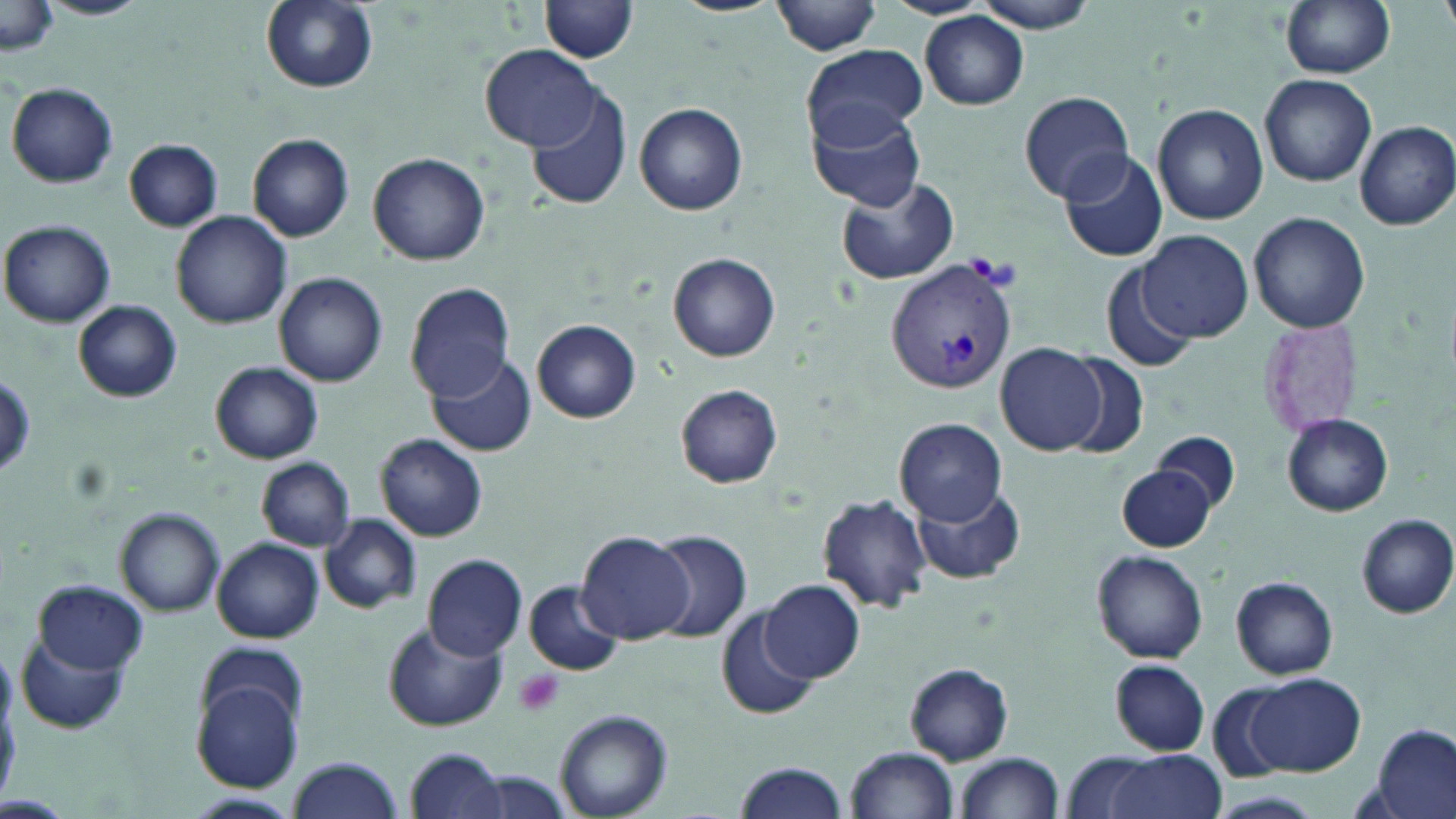

slide-level diagnosis = Plasmodium vivax
image size = 1456×819 pixels
field of view = one of a larger specimen
platelet locations = approximate bounding boxes as [x1, y1, x2, y2] in pixels: [512, 667, 565, 719]
uninfected red blood cell locations = approximate bounding boxes as [x1, y1, x2, y2] in pixels: [41, 0, 148, 20], [259, 0, 378, 92], [1279, 0, 1393, 79], [540, 1, 639, 63], [771, 1, 883, 55], [971, 1, 1102, 33], [1, 2, 61, 60], [920, 13, 1030, 109], [481, 43, 599, 149], [802, 43, 927, 150], [1259, 72, 1377, 186], [6, 80, 117, 188], [525, 85, 635, 212], [1020, 90, 1135, 203], [635, 102, 749, 214], [1153, 103, 1269, 223], [809, 106, 928, 210], [1354, 121, 1456, 231], [247, 133, 354, 241], [125, 141, 223, 230], [1058, 147, 1167, 263], [368, 151, 491, 265], [836, 175, 959, 286], [1247, 211, 1370, 334], [171, 212, 293, 328], [1, 219, 118, 327], [1139, 230, 1252, 342], [668, 252, 781, 361], [1099, 259, 1201, 374], [275, 273, 388, 387], [406, 283, 514, 401], [74, 300, 181, 402], [533, 318, 642, 422], [995, 343, 1104, 455], [428, 351, 536, 457], [1057, 353, 1152, 461], [209, 361, 323, 465], [0, 368, 34, 481], [676, 384, 782, 488], [1282, 415, 1393, 516], [895, 416, 1007, 525], [1153, 431, 1241, 515], [376, 434, 487, 542], [257, 457, 354, 551], [1116, 465, 1217, 551], [912, 481, 1024, 585], [816, 495, 933, 613], [114, 506, 226, 617], [1356, 513, 1456, 619], [319, 514, 422, 614], [648, 530, 752, 644], [577, 531, 694, 644], [213, 537, 324, 643], [1093, 549, 1209, 663], [424, 553, 528, 661], [1229, 576, 1339, 680], [760, 578, 865, 684], [35, 581, 147, 675], [525, 583, 622, 676], [717, 607, 821, 723], [383, 618, 506, 730], [15, 627, 132, 736], [1109, 661, 1209, 755], [904, 662, 1014, 763], [193, 672, 304, 794], [1244, 673, 1364, 774], [555, 710, 671, 819], [1370, 724, 1455, 819], [847, 746, 960, 818], [406, 748, 508, 819], [953, 752, 1065, 819], [1096, 752, 1223, 819], [288, 757, 404, 819], [731, 762, 843, 819], [475, 771, 571, 818], [1209, 791, 1324, 818], [187, 792, 304, 816]
stain = May-Grünwald-Giemsa
magnification = 1000x
Plasmodium vivax-infected red blood cell locations = approximate bounding boxes as [x1, y1, x2, y2] in pixels: [885, 259, 1018, 398]
preparation = thin blood film
modality = optical microscopy